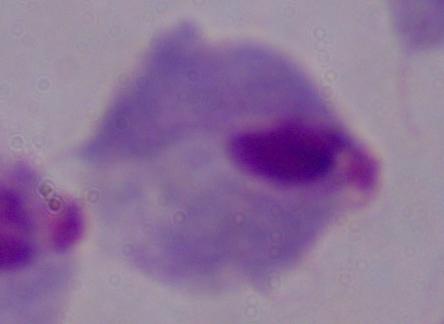
identification = trichomonad
magnification = 1000x
modality = micrograph